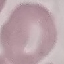
Summary:
  - Malaria status: uninfected
  - Capture: smartphone camera at the microscope eyepiece
  - Preparation: thin blood film
  - Stain: Giemsa
  - Image type: cell patch, automatically extracted from a larger field of view and resized to 64 × 64 pixels